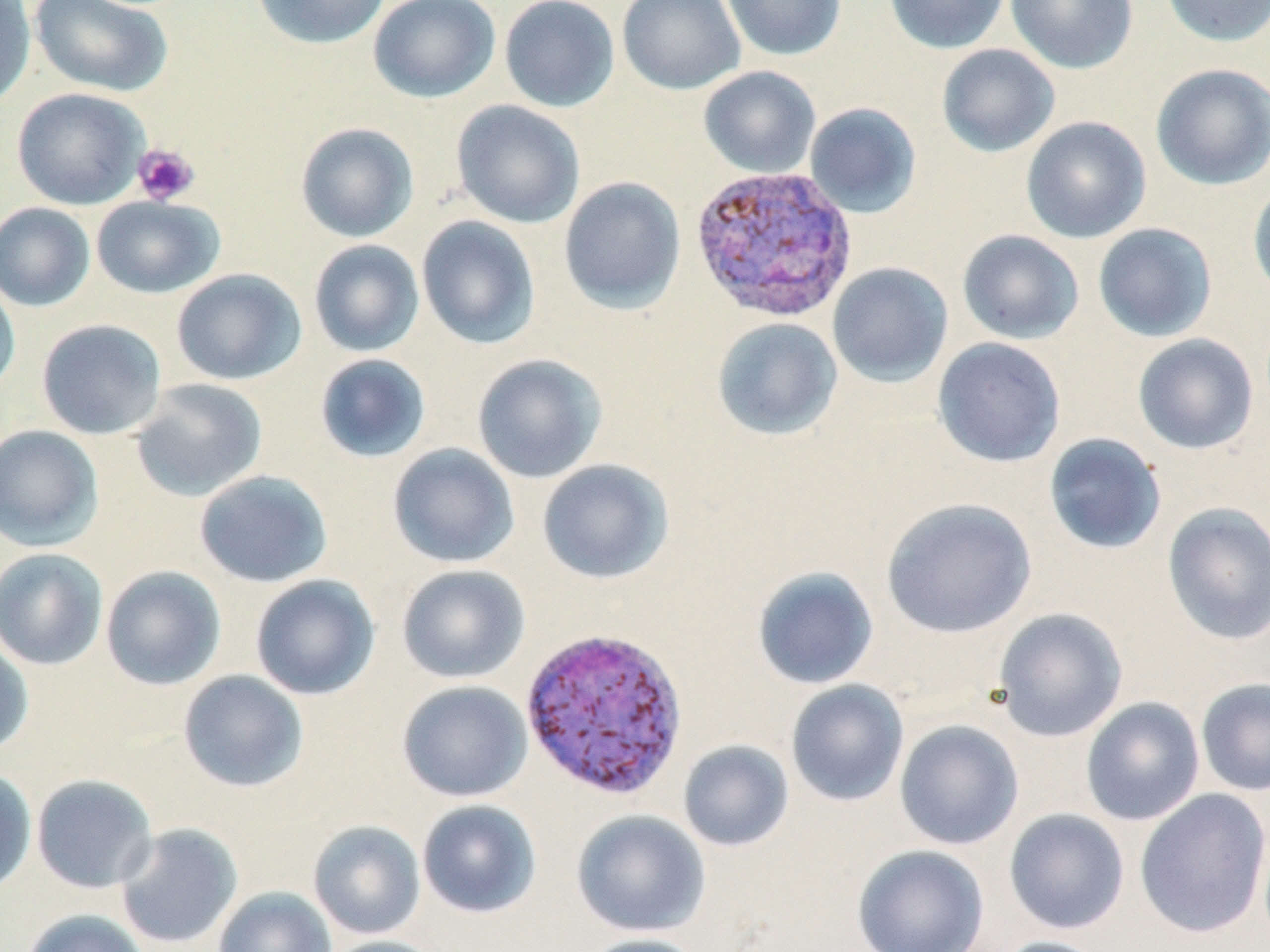
Approximate bounding boxes as (x1,y1)-(x2,y2) corner pairs in pixels. Uninfected red blood cell locations: (0,0)-(36,111), (29,0)-(173,98), (252,0)-(391,49), (367,0)-(501,103), (499,0)-(620,112), (617,0)-(745,95), (721,0)-(847,61), (884,0)-(1010,54), (1005,0)-(1138,75), (1160,0)-(1270,47), (936,44)-(1060,157), (1151,64)-(1270,190), (698,66)-(821,178), (11,86)-(149,210), (451,100)-(585,228), (804,102)-(922,218), (1020,116)-(1151,244), (295,122)-(418,242), (558,176)-(686,314), (1248,180)-(1270,303), (91,195)-(224,298), (0,202)-(96,312), (416,216)-(541,349), (1092,223)-(1217,342), (957,229)-(1084,345), (308,239)-(424,357), (827,262)-(953,388), (171,268)-(307,386), (0,277)-(21,396), (712,317)-(843,441), (36,318)-(167,440), (1132,333)-(1259,455), (932,337)-(1066,468), (314,353)-(431,463), (472,354)-(607,483), (130,378)-(268,502), (0,424)-(103,552), (1043,432)-(1167,555), (387,443)-(520,569), (537,459)-(674,585), (194,469)-(333,588), (880,497)-(1037,638), (1161,502)-(1270,645), (0,548)-(108,670), (397,564)-(530,684), (100,565)-(226,691), (751,566)-(879,690), (249,574)-(380,700), (992,608)-(1127,742), (0,637)-(34,756), (178,670)-(309,793), (1195,677)-(1270,797), (785,679)-(909,807), (397,681)-(532,802), (1080,697)-(1205,826), (894,719)-(1024,850), (678,739)-(794,852), (0,767)-(37,896), (31,774)-(158,893), (1133,788)-(1270,939), (417,799)-(541,918), (1003,808)-(1130,934), (571,809)-(711,938), (308,820)-(426,939), (114,822)-(244,950), (852,844)-(990,952), (213,886)-(337,952), (19,908)-(151,952), (575,934)-(709,952), (319,935)-(448,952), (989,936)-(1113,952). Platelet locations: (133,143)-(200,206). Plasmodium vivax-infected red blood cell locations: (688,165)-(859,324), (519,625)-(689,802). Slide-level diagnosis: Plasmodium vivax. May-Grünwald-Giemsa stain. Captured at 1000x magnification. Optical microscopy. Thin blood film. Single field of view. Image is 1270×952 pixels.